Report the malaria status of this cell.
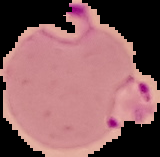

It is parasitized.

preparation = thin blood smear
image size = 160×157 pixels
image type = segmented cell region with the area outside set to black